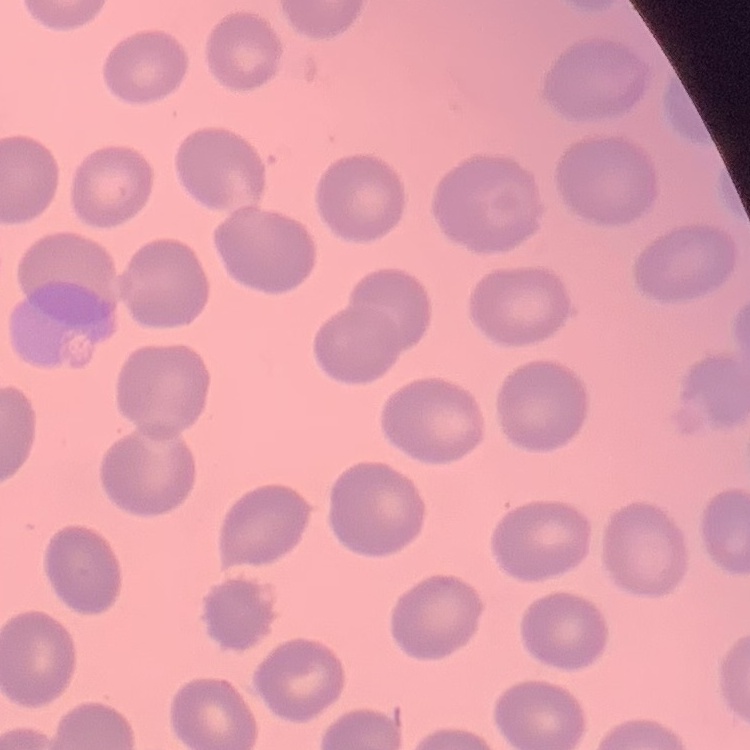
Summary:
  - Red blood cell morphology: no rouleaux formation
  - Stain: Field's or Giemsa
  - Preparation: thin peripheral smear
  - Image type: one tile cut from a larger photomicrograph